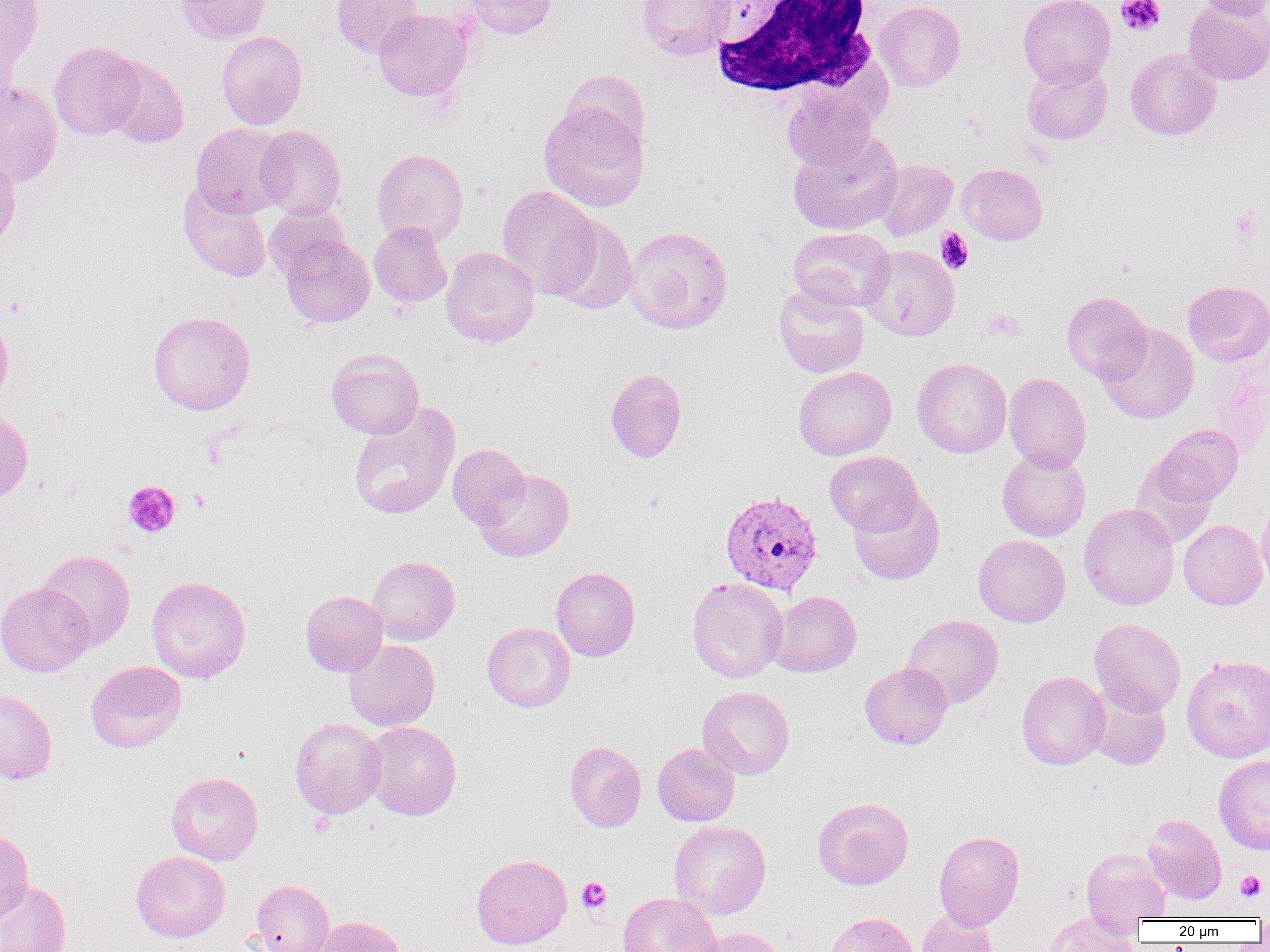
Summary:
  - Coordinate format: approximate bounding boxes as named x1/y1/x2/y2 corners in pixels
  - Plasmodium vivax-infected red blood cell locations: (x1=720, y1=489, x2=824, y2=595)
  - Platelet locations: (x1=1116, y1=0, x2=1166, y2=36), (x1=1230, y1=208, x2=1264, y2=248), (x1=936, y1=228, x2=974, y2=274), (x1=985, y1=309, x2=1025, y2=341), (x1=123, y1=480, x2=180, y2=538), (x1=1235, y1=870, x2=1267, y2=901), (x1=577, y1=877, x2=611, y2=914)
  - White blood cell locations: (x1=710, y1=1, x2=879, y2=100)
  - Uninfected red blood cell locations: (x1=1, y1=0, x2=43, y2=80), (x1=175, y1=0, x2=271, y2=44), (x1=332, y1=0, x2=422, y2=58), (x1=463, y1=0, x2=558, y2=39), (x1=638, y1=0, x2=734, y2=59), (x1=1018, y1=0, x2=1115, y2=88), (x1=1198, y1=0, x2=1269, y2=20), (x1=874, y1=1, x2=965, y2=91), (x1=1184, y1=1, x2=1270, y2=85), (x1=373, y1=9, x2=471, y2=101), (x1=216, y1=31, x2=307, y2=130), (x1=48, y1=41, x2=145, y2=139), (x1=1125, y1=48, x2=1221, y2=140), (x1=102, y1=56, x2=189, y2=148), (x1=1023, y1=64, x2=1112, y2=144), (x1=559, y1=69, x2=649, y2=155), (x1=0, y1=80, x2=63, y2=187), (x1=782, y1=85, x2=878, y2=171), (x1=539, y1=100, x2=649, y2=212), (x1=190, y1=122, x2=289, y2=217), (x1=255, y1=125, x2=346, y2=220), (x1=788, y1=130, x2=904, y2=235), (x1=372, y1=148, x2=468, y2=246), (x1=0, y1=151, x2=21, y2=254), (x1=875, y1=160, x2=957, y2=241), (x1=958, y1=163, x2=1047, y2=245), (x1=178, y1=182, x2=272, y2=282), (x1=497, y1=185, x2=600, y2=298), (x1=263, y1=204, x2=350, y2=280), (x1=548, y1=216, x2=638, y2=314), (x1=369, y1=222, x2=452, y2=308), (x1=624, y1=226, x2=733, y2=334), (x1=788, y1=227, x2=895, y2=311), (x1=280, y1=235, x2=375, y2=327), (x1=861, y1=245, x2=959, y2=341), (x1=440, y1=246, x2=539, y2=347), (x1=1183, y1=281, x2=1270, y2=366), (x1=774, y1=284, x2=869, y2=378), (x1=1062, y1=291, x2=1152, y2=383), (x1=147, y1=311, x2=256, y2=415), (x1=0, y1=312, x2=13, y2=407), (x1=1097, y1=324, x2=1199, y2=424), (x1=327, y1=348, x2=424, y2=439), (x1=912, y1=357, x2=1012, y2=458), (x1=793, y1=366, x2=896, y2=460), (x1=605, y1=368, x2=687, y2=463), (x1=1003, y1=372, x2=1091, y2=473), (x1=348, y1=402, x2=461, y2=520), (x1=0, y1=412, x2=33, y2=503), (x1=1149, y1=424, x2=1243, y2=510), (x1=447, y1=443, x2=531, y2=530), (x1=997, y1=448, x2=1090, y2=542), (x1=825, y1=450, x2=923, y2=535), (x1=474, y1=468, x2=574, y2=562), (x1=849, y1=490, x2=944, y2=585), (x1=1256, y1=497, x2=1270, y2=591), (x1=1078, y1=502, x2=1179, y2=610), (x1=1178, y1=520, x2=1267, y2=610), (x1=973, y1=534, x2=1071, y2=627), (x1=37, y1=550, x2=135, y2=649), (x1=368, y1=556, x2=459, y2=645), (x1=551, y1=567, x2=640, y2=661), (x1=147, y1=576, x2=251, y2=683), (x1=687, y1=577, x2=788, y2=683), (x1=0, y1=582, x2=95, y2=677), (x1=769, y1=590, x2=861, y2=677), (x1=300, y1=591, x2=388, y2=676), (x1=902, y1=614, x2=1003, y2=709), (x1=1089, y1=618, x2=1185, y2=716), (x1=482, y1=622, x2=575, y2=712), (x1=344, y1=639, x2=440, y2=731), (x1=1181, y1=655, x2=1270, y2=762), (x1=86, y1=660, x2=186, y2=752), (x1=860, y1=662, x2=952, y2=750), (x1=1016, y1=671, x2=1109, y2=770), (x1=1087, y1=685, x2=1171, y2=770), (x1=697, y1=686, x2=795, y2=779), (x1=0, y1=689, x2=57, y2=784), (x1=289, y1=718, x2=386, y2=819), (x1=363, y1=721, x2=462, y2=820), (x1=565, y1=741, x2=646, y2=832), (x1=652, y1=742, x2=740, y2=826), (x1=1214, y1=755, x2=1270, y2=854), (x1=166, y1=772, x2=263, y2=865), (x1=813, y1=798, x2=913, y2=890), (x1=1142, y1=814, x2=1227, y2=904), (x1=669, y1=820, x2=771, y2=919), (x1=0, y1=829, x2=33, y2=923), (x1=934, y1=831, x2=1024, y2=930), (x1=1081, y1=849, x2=1170, y2=924), (x1=131, y1=850, x2=231, y2=942), (x1=471, y1=854, x2=572, y2=949), (x1=0, y1=879, x2=72, y2=952), (x1=251, y1=880, x2=334, y2=952), (x1=618, y1=892, x2=722, y2=952), (x1=915, y1=908, x2=1000, y2=952), (x1=1042, y1=911, x2=1141, y2=951), (x1=822, y1=912, x2=919, y2=952), (x1=313, y1=916, x2=407, y2=952), (x1=698, y1=927, x2=792, y2=952)
  - Slide-level diagnosis: Plasmodium vivax
  - Modality: optical microscopy
  - Magnification: 1000x
  - Field of view: one of a larger specimen
  - Image size: 1270×952 pixels
  - Preparation: thin blood film